Comment on the morphology of the red blood cells.
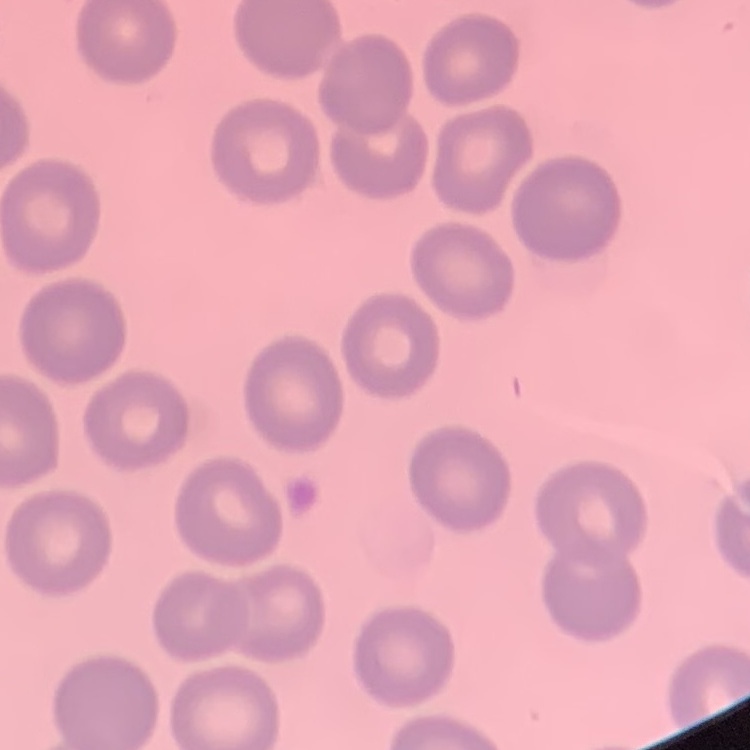
They show no rouleaux formation.

Thin blood film. Square crop of a larger photomicrograph. Field's or Giemsa stain.